Comment on the morphology of the red blood cells.
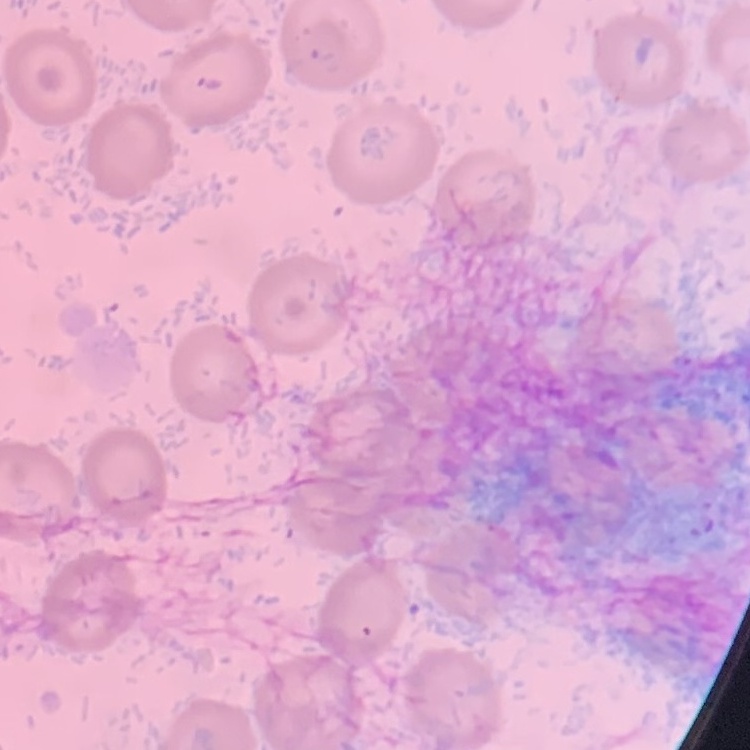

No rouleaux formation.

Summary:
  - Image type: square crop of a larger photomicrograph
  - Preparation: thin blood film
  - Stain: Field's or Giemsa